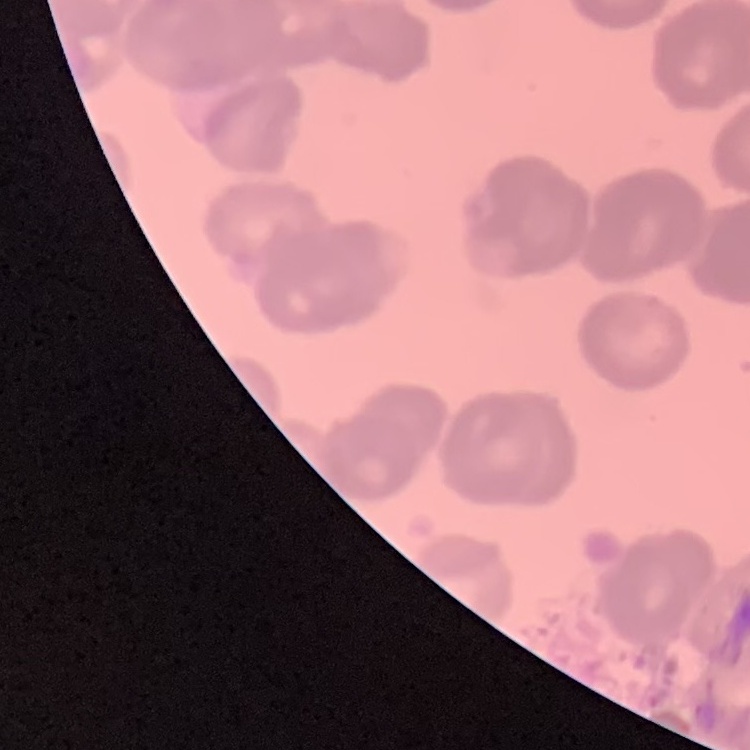

The red blood cells exhibit rouleaux formation. Field's or Giemsa stain. Square crop of a larger photomicrograph. Thin blood film.